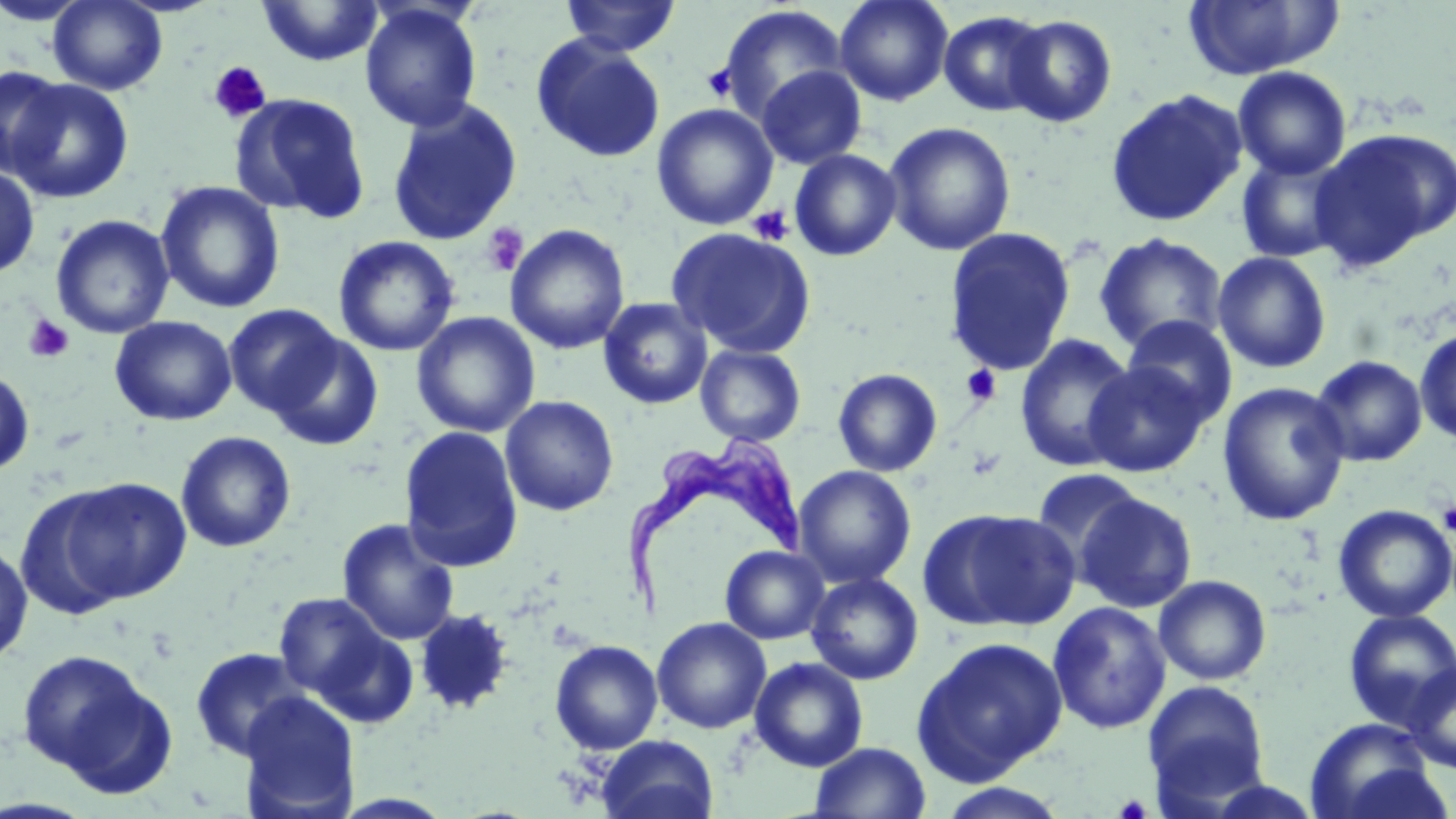

Summary:
  - Coordinate format: approximate bounding boxes as (x1, y1, x2, y2) in pixels
  - Uninfected red blood cell locations: (48, 0, 167, 95), (560, 0, 681, 56), (834, 0, 954, 106), (257, 1, 384, 66), (1182, 1, 1339, 80), (359, 3, 482, 132), (717, 5, 849, 124), (938, 10, 1052, 117), (1003, 14, 1117, 127), (532, 35, 665, 163), (0, 65, 70, 177), (755, 65, 867, 170), (1232, 66, 1351, 180), (5, 78, 134, 203), (1105, 89, 1248, 228), (231, 92, 371, 224), (385, 99, 523, 245), (651, 103, 778, 230), (883, 121, 1016, 256), (1311, 128, 1456, 266), (789, 148, 902, 261), (1235, 152, 1352, 264), (0, 163, 40, 279), (155, 180, 285, 314), (51, 214, 175, 339), (504, 224, 630, 355), (666, 226, 815, 358), (943, 226, 1076, 377), (1093, 232, 1228, 354), (333, 235, 460, 357), (1212, 251, 1331, 373), (598, 297, 713, 409), (224, 304, 343, 417), (411, 312, 540, 438), (1122, 315, 1238, 424), (110, 316, 236, 426), (1414, 327, 1456, 447), (267, 332, 384, 451), (1014, 333, 1138, 473), (695, 344, 806, 447), (1310, 354, 1428, 467), (1084, 361, 1210, 477), (0, 368, 35, 477), (833, 368, 942, 477), (1217, 381, 1351, 526), (500, 395, 619, 516), (399, 425, 524, 573), (175, 431, 296, 553), (794, 465, 916, 588), (1032, 467, 1145, 568), (54, 477, 192, 605), (1075, 492, 1197, 614), (1332, 504, 1456, 623), (920, 508, 1080, 632), (336, 518, 460, 646), (0, 538, 33, 667), (720, 545, 829, 645), (806, 572, 924, 685), (1153, 574, 1272, 685), (273, 591, 411, 722), (1047, 601, 1171, 735), (413, 608, 514, 716), (1342, 608, 1456, 730), (652, 617, 771, 734), (912, 636, 1068, 784), (550, 639, 663, 755), (189, 646, 311, 762), (15, 648, 171, 792), (749, 656, 868, 772), (1404, 662, 1456, 774), (1142, 679, 1271, 810), (238, 692, 361, 818), (1305, 716, 1439, 818), (596, 734, 719, 819), (809, 741, 931, 819), (936, 782, 1071, 819)
  - Trypanosoma brucei locations: (626, 428, 805, 620)
  - Platelet locations: (208, 61, 272, 123), (703, 63, 739, 101), (748, 206, 794, 246), (481, 222, 528, 276), (23, 314, 74, 363), (961, 365, 1002, 406), (1437, 501, 1456, 535), (1114, 794, 1152, 819)
  - Slide-level diagnosis: Trypanosoma brucei
  - Preparation: thin blood film
  - Modality: optical microscopy
  - Field of view: one of a larger specimen
  - Image size: 1456×819 pixels
  - Stain: May-Grünwald-Giemsa
  - Magnification: 1000x